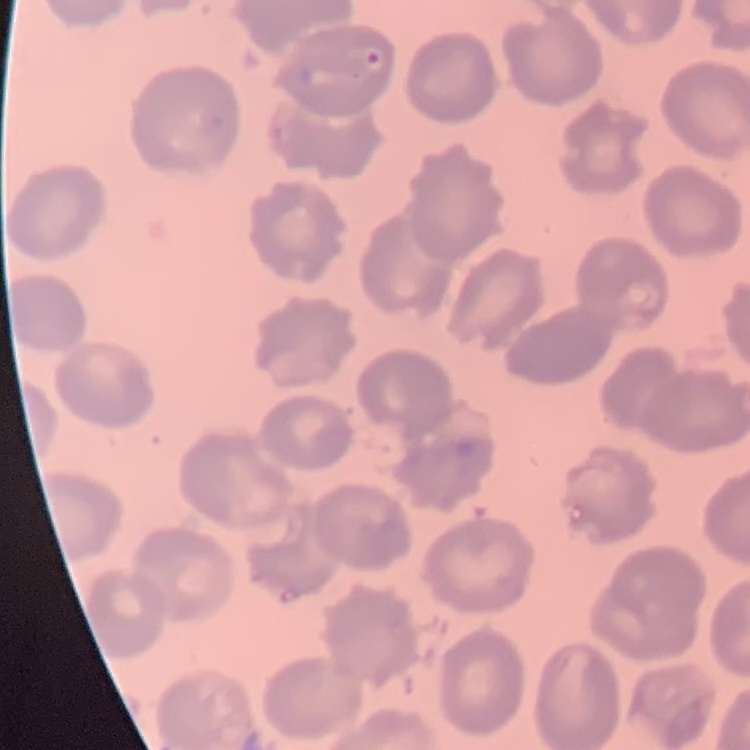
Summary:
  - Erythrocyte morphology: no rouleaux formation
  - Image type: one tile cut from a larger photomicrograph
  - Preparation: thin blood film
  - Stain: Field's or Giemsa